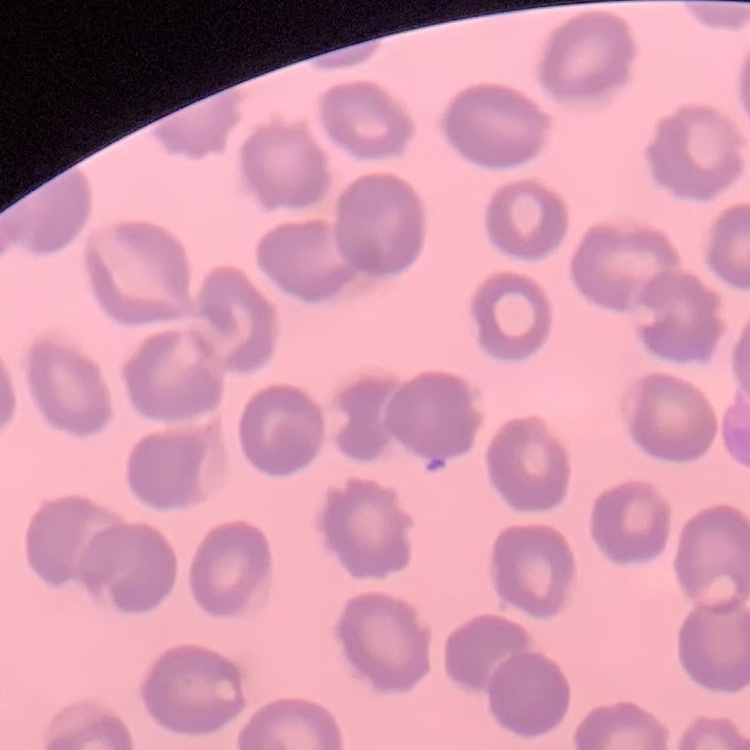

The red blood cells show no rouleaux formation. Thin peripheral smear. Stained with either Field's or Giemsa. Square crop of a larger photomicrograph.